Give the extent of all Plasmodium falciparum-infected red blood cells.
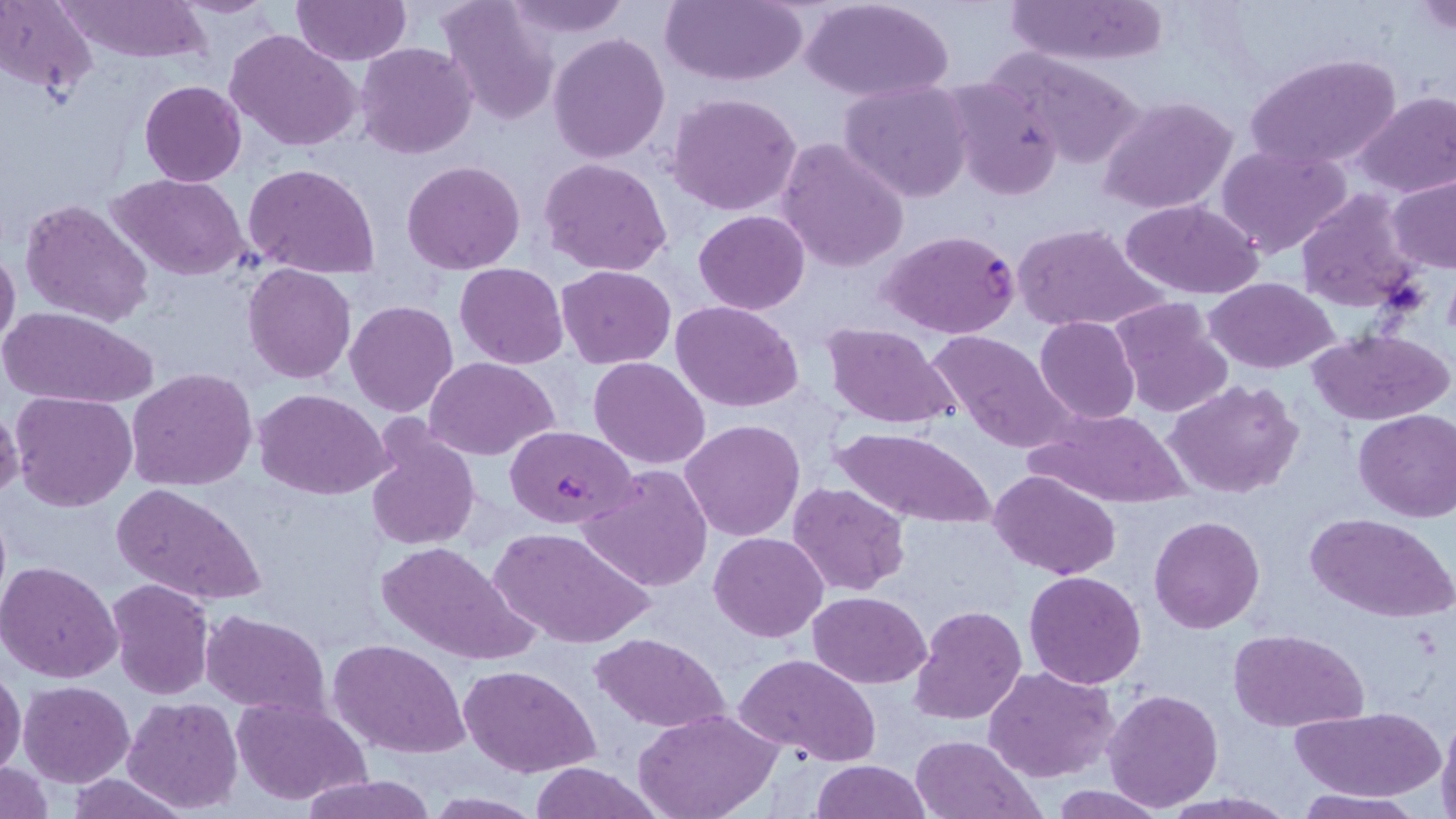
Approximate bounding boxes as (x1,y1)-(x2,y2) corner pairs in pixels.
Plasmodium falciparum-infected red blood cells: (878,230)-(1020,339), (509,418)-(638,525).

Uninfected red blood cell locations: (57,0)-(212,63), (170,0)-(282,19), (439,0)-(559,125), (501,0)-(632,39), (662,0)-(811,87), (800,0)-(954,102), (1003,0)-(1168,67), (1413,0)-(1455,36), (0,1)-(97,92), (291,1)-(410,66), (226,28)-(364,152), (549,32)-(671,162), (355,42)-(478,159), (995,49)-(1147,168), (1248,54)-(1400,172), (940,74)-(1067,200), (140,80)-(247,186), (839,80)-(973,203), (1353,90)-(1456,199), (666,92)-(803,216), (1098,95)-(1237,215), (776,137)-(909,274), (1218,144)-(1352,258), (540,157)-(672,276), (402,160)-(526,274), (246,164)-(382,279), (109,172)-(250,280), (1386,172)-(1456,273), (1295,189)-(1422,314), (20,196)-(153,327), (1119,198)-(1265,300), (693,210)-(808,313), (1011,221)-(1167,333), (0,243)-(20,356), (455,262)-(568,367), (568,262)-(689,463), (242,264)-(357,383), (555,265)-(677,368), (1202,278)-(1342,374), (1109,298)-(1233,420), (346,300)-(459,417), (670,300)-(804,415), (1,306)-(158,408), (1035,316)-(1140,424), (820,321)-(961,430), (926,328)-(1078,454), (1305,329)-(1453,426), (425,356)-(559,460), (589,357)-(711,470), (126,368)-(258,493), (1164,380)-(1305,500), (253,389)-(391,498), (11,390)-(136,512), (1029,407)-(1192,507), (1354,408)-(1455,522), (364,417)-(481,551), (679,420)-(805,541), (833,426)-(996,529), (580,465)-(713,592), (989,469)-(1123,580), (786,481)-(911,598), (113,484)-(265,608), (1306,512)-(1456,623), (1149,515)-(1264,634), (487,526)-(653,650), (708,532)-(829,642), (375,540)-(533,665), (0,560)-(123,683), (1023,571)-(1147,689), (107,578)-(214,700), (806,591)-(932,688), (909,605)-(1028,726), (200,609)-(330,713), (945,617)-(1113,755), (1229,628)-(1369,730), (593,631)-(730,730), (327,637)-(471,758), (610,638)-(750,807), (734,653)-(882,767), (459,664)-(600,778), (0,665)-(26,778), (985,666)-(1117,783), (19,681)-(135,786), (1101,687)-(1223,812), (230,694)-(372,806), (122,698)-(243,814), (1292,708)-(1442,801), (633,709)-(780,819), (1436,713)-(1456,819), (909,734)-(1040,818), (811,759)-(930,819), (0,761)-(52,818), (527,763)-(663,819), (299,773)-(439,819), (66,774)-(193,817), (1047,785)-(1171,817), (1293,789)-(1423,818), (421,793)-(546,817). Slide-level diagnosis: Plasmodium falciparum. Single field of view. Image is 1456×819 pixels. Light microscopy. Captured at 1000x magnification. Thin blood film. May-Grünwald-Giemsa-stained preparation.